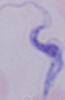

Summary:
  - Magnification: 1000x
  - Identification: trypanosome
  - Modality: micrograph